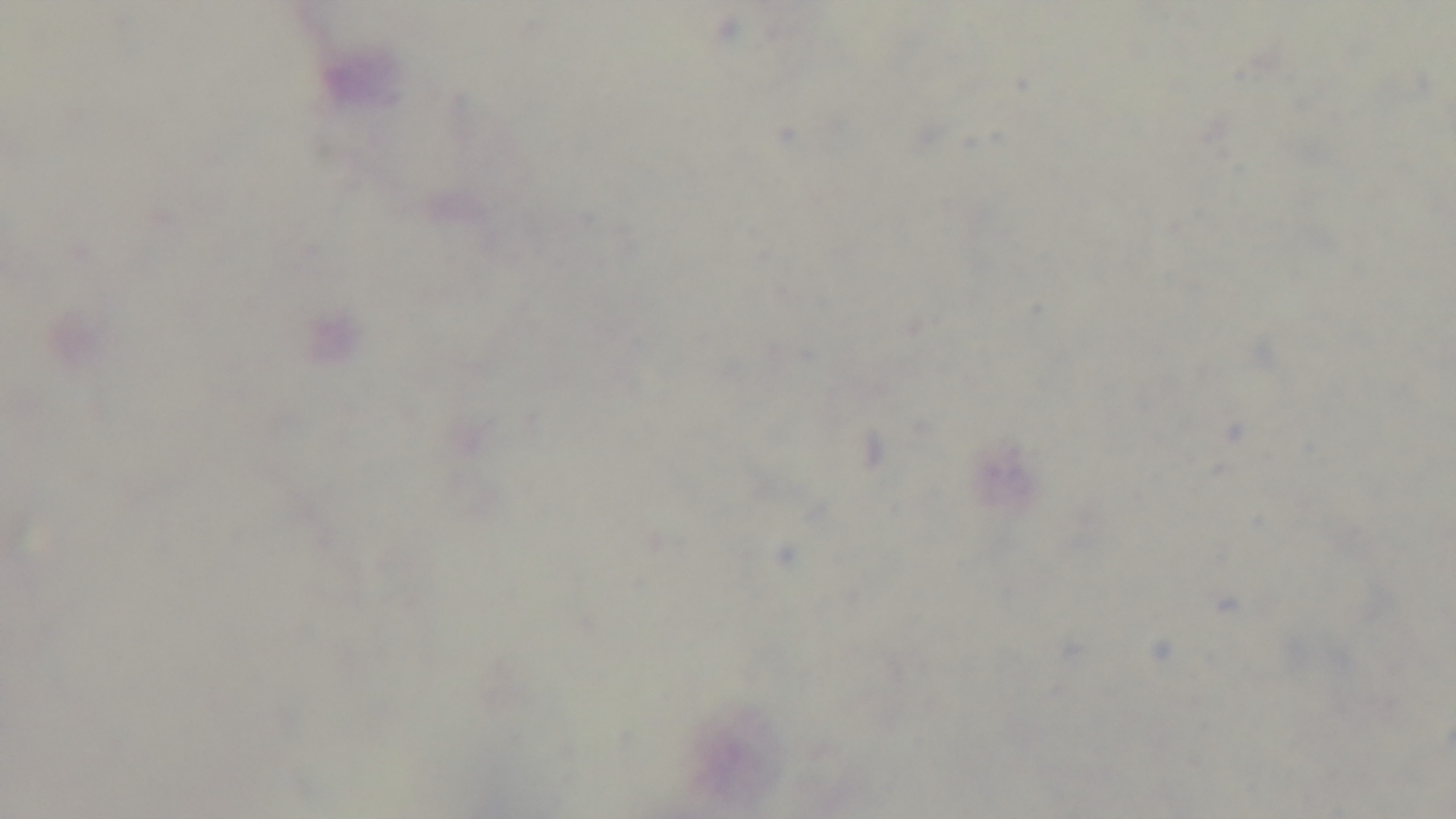
field_of_view: one from the slide
modality: light microscopy
stain: Giemsa
capture: mounted 4K digital camera
malaria_status: negative
preparation: thick
objective: 100x oil immersion